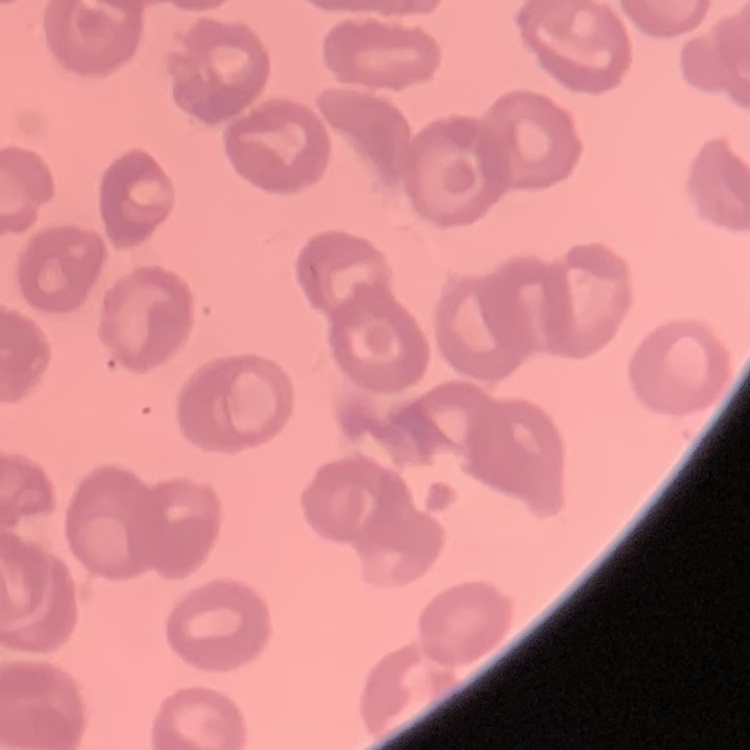
The red blood cells show no rouleaux formation. One tile cut from a larger photomicrograph. Stained with either Field's or Giemsa. Thin blood film.